Describe the morphology of the red blood cells.
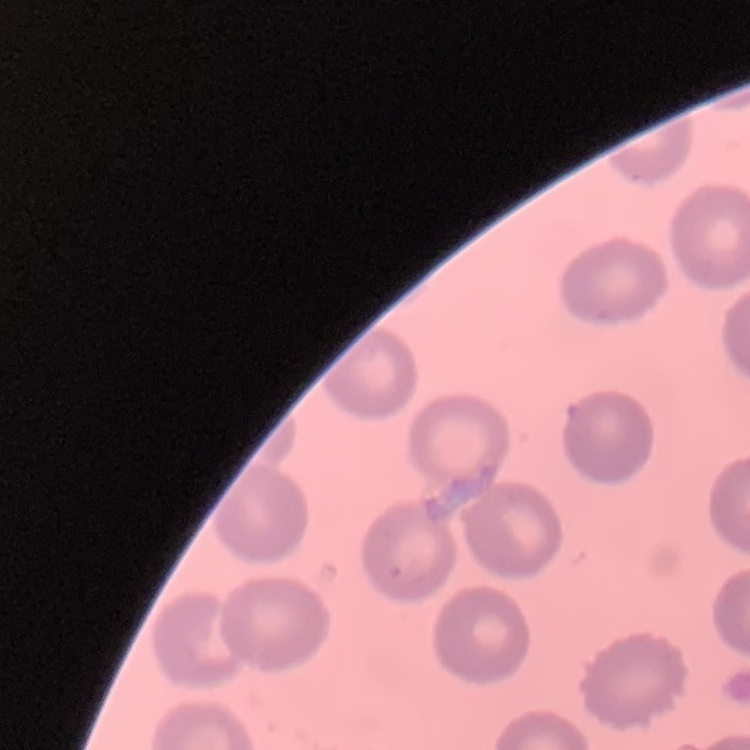

They show no rouleaux formation.

Summary:
  - Stain: Field's or Giemsa
  - Preparation: thin blood smear
  - Image type: one tile cut from a larger photomicrograph